Name the parasite shown.
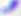

Toxoplasma gondii.

{
  "modality": "photomicrograph",
  "magnification": "400x"
}